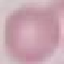

malaria status = uninfected
stain = Giemsa
image type = cell patch, automatically extracted from a larger field of view and resized to 64 × 64 pixels
capture = smartphone camera at the microscope eyepiece
preparation = thin smear